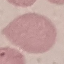
Summary:
  - Result: negative for malaria parasites
  - Preparation: thin blood film
  - Capture: smartphone through the microscope eyepiece
  - Image type: cell patch, automatically extracted from a larger field of view and resized to 64 × 64 pixels
  - Stain: Giemsa